Outline each blood parasite and name the species.
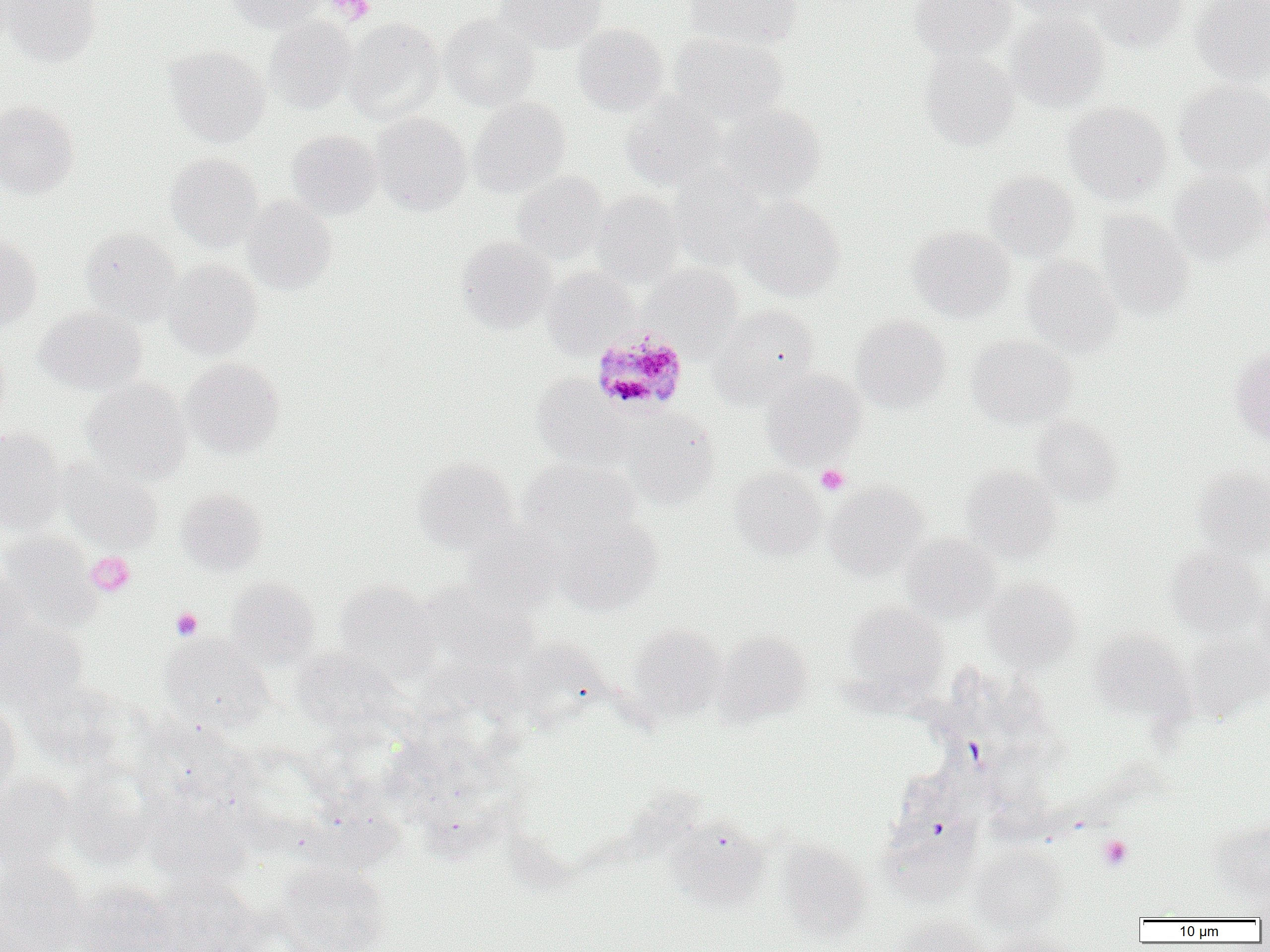
Approximate bounding boxes as [x1, y1, x2, y2] in pixels.
Plasmodium malariae-infected red blood cells: [595, 329, 693, 414].
No Plasmodium falciparum, Plasmodium ovale, Plasmodium vivax, Babesia divergens, or Trypanosoma brucei observed.

slide_level_diagnosis: Plasmodium malariae
field_of_view: single
preparation: thin blood film
modality: light microscopy
image_size: 1270×952 pixels
platelet_locations: 'approximate bounding boxes as [x1, y1, x2, y2] in pixels: [329, 0, 374, 24], [816, 465, 850, 494], [86, 551, 135, 596], [170, 607, 203, 640], [1098, 835, 1132, 870]'
magnification: 1000x
uninfected_red_blood_cell_locations: 'approximate bounding boxes as [x1, y1, x2, y2] in pixels: [3, 0, 102, 66], [226, 0, 324, 33], [497, 0, 606, 52], [684, 0, 803, 49], [909, 0, 1016, 61], [1006, 0, 1111, 21], [1090, 0, 1189, 52], [1190, 0, 1270, 84], [1007, 10, 1110, 112], [439, 13, 539, 111], [265, 17, 357, 113], [345, 18, 444, 124], [573, 24, 669, 114], [670, 33, 788, 126], [164, 45, 270, 147], [919, 49, 1020, 150], [1175, 80, 1270, 176], [622, 94, 725, 191], [469, 98, 571, 197], [0, 101, 80, 198], [1063, 102, 1171, 204], [715, 103, 827, 201], [371, 112, 472, 215], [287, 129, 382, 219], [165, 153, 263, 251], [669, 166, 771, 269], [512, 170, 609, 264], [982, 170, 1079, 262], [1169, 170, 1267, 261], [592, 191, 684, 287], [242, 195, 337, 295], [737, 196, 844, 300], [1096, 210, 1194, 320], [907, 225, 1016, 323], [80, 227, 182, 325], [0, 235, 42, 330], [456, 236, 556, 333], [1020, 255, 1123, 356], [163, 259, 261, 358], [643, 263, 744, 354], [542, 266, 637, 358], [712, 304, 821, 403], [35, 307, 146, 394], [851, 315, 952, 412], [966, 335, 1075, 428], [0, 338, 11, 432], [1230, 346, 1270, 445], [181, 357, 285, 458], [761, 369, 867, 468], [532, 375, 629, 469], [81, 379, 192, 485], [624, 412, 720, 508], [1030, 417, 1122, 505], [0, 428, 66, 535], [412, 456, 519, 555], [57, 457, 164, 552], [518, 457, 640, 543], [729, 466, 826, 559], [962, 466, 1063, 562], [1191, 466, 1270, 558], [824, 483, 929, 579], [174, 487, 268, 575], [557, 514, 664, 614], [463, 521, 565, 613], [901, 533, 1001, 622], [1, 534, 101, 631], [1166, 546, 1266, 638], [0, 568, 35, 660], [225, 577, 320, 670], [982, 578, 1081, 671], [335, 580, 440, 683], [418, 580, 538, 672], [1253, 581, 1270, 681], [843, 602, 948, 695], [0, 613, 87, 710], [627, 623, 728, 720], [1088, 630, 1195, 724], [715, 631, 814, 726], [1184, 633, 1269, 722], [160, 636, 274, 734], [290, 647, 407, 740], [25, 679, 141, 772], [0, 702, 22, 803], [137, 717, 253, 813], [62, 762, 160, 868], [0, 772, 77, 871], [142, 790, 255, 888], [667, 818, 770, 910], [1208, 818, 1270, 901], [776, 841, 872, 942], [970, 846, 1068, 934], [0, 856, 88, 952], [274, 861, 392, 952], [1254, 875, 1270, 923], [152, 876, 264, 952], [73, 881, 181, 952], [890, 915, 989, 952], [986, 927, 1075, 952]'